Outline each Plasmodium malariae-infected red blood cell.
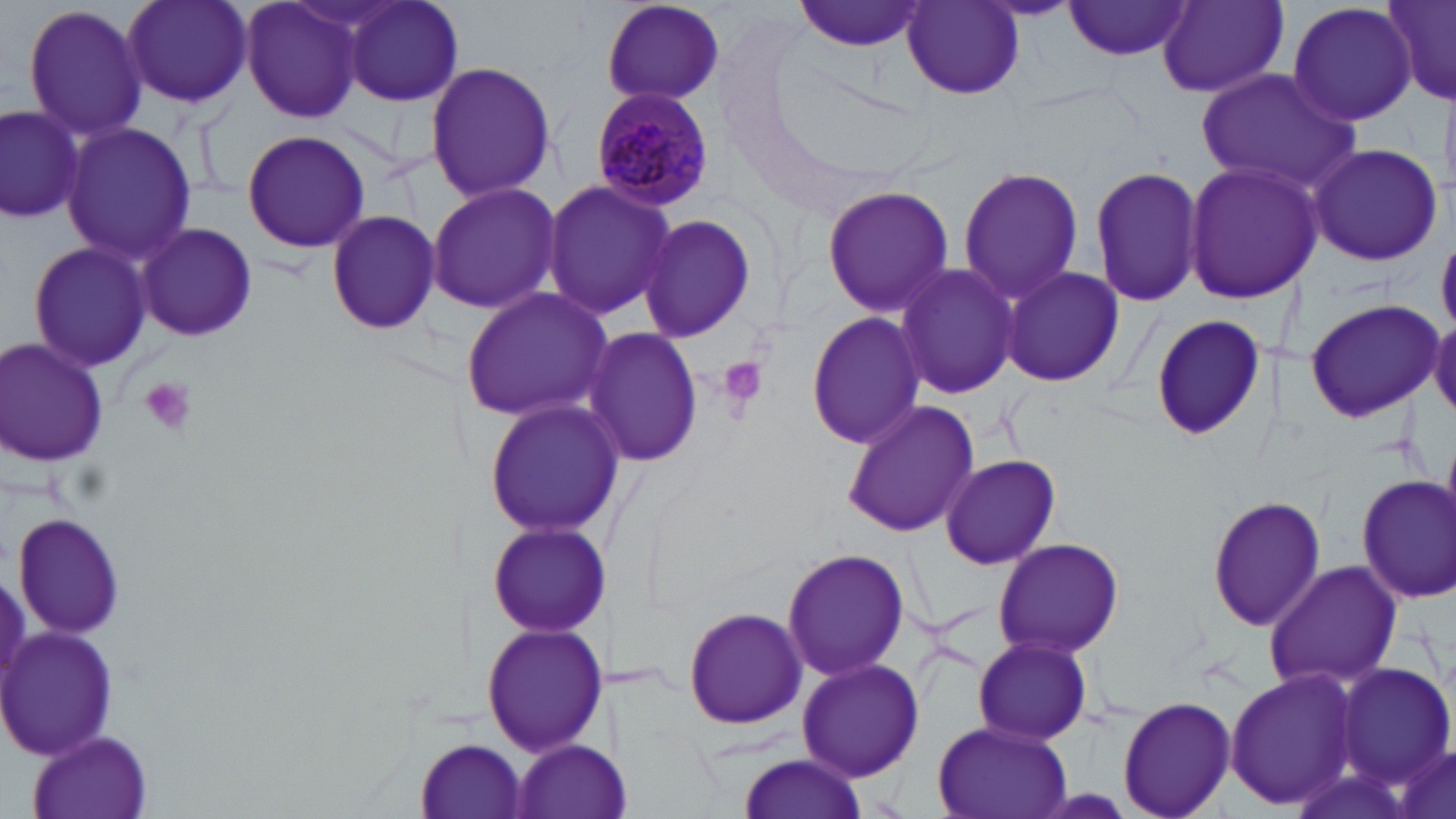
Approximate bounding boxes as (x1, y1, x2, y2) in pixels.
Plasmodium malariae-infected red blood cells: (589, 85, 716, 211).

Summary:
  - Platelet locations: (717, 355, 766, 414), (138, 375, 197, 437)
  - Uninfected red blood cell locations (subset): (118, 0, 255, 109), (338, 0, 466, 109), (793, 0, 927, 53), (1386, 0, 1456, 101), (239, 1, 368, 123), (597, 1, 726, 107), (1063, 1, 1194, 61), (20, 2, 152, 143), (1158, 2, 1287, 97), (1286, 2, 1420, 127), (901, 4, 1025, 99), (425, 60, 559, 202), (1195, 68, 1360, 194), (0, 103, 84, 229), (63, 123, 194, 265), (241, 130, 372, 252), (1304, 141, 1444, 269), (1182, 159, 1322, 305), (1089, 165, 1205, 308), (958, 167, 1086, 302), (542, 177, 676, 323), (425, 179, 561, 316), (821, 184, 954, 319), (325, 207, 443, 336), (639, 212, 759, 345), (134, 223, 257, 343), (26, 239, 154, 374), (893, 264, 1023, 399), (1000, 264, 1126, 389), (459, 286, 616, 424), (1302, 296, 1442, 424), (1429, 310, 1456, 420), (804, 312, 925, 448), (1149, 314, 1267, 442), (582, 325, 704, 471), (1, 337, 109, 466), (481, 397, 625, 541), (842, 398, 980, 541), (940, 453, 1064, 572), (1354, 473, 1456, 606), (1206, 493, 1326, 634), (12, 513, 130, 640), (486, 521, 609, 640), (991, 536, 1126, 659), (781, 548, 910, 684), (1263, 560, 1402, 691), (683, 604, 808, 731), (480, 621, 606, 758), (972, 635, 1093, 745), (796, 657, 923, 782), (1337, 661, 1454, 790), (1223, 665, 1362, 813), (1116, 695, 1236, 819), (932, 720, 1071, 819), (26, 731, 156, 818), (412, 737, 531, 819), (1389, 738, 1454, 819), (511, 739, 619, 819), (735, 753, 869, 819)
  - Slide-level diagnosis: Plasmodium malariae
  - Preparation: thin blood film
  - Field of view: one of a larger specimen
  - Modality: light microscopy
  - Stain: May-Grünwald-Giemsa
  - Image size: 1456×819 pixels
  - Magnification: 1000x